Assess this cell for malaria.
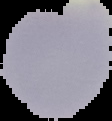

Uninfected.

image size = 112×121 pixels
preparation = thin blood smear
image type = segmented cell region with the area outside set to black